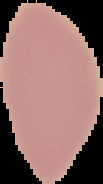

{
  "malaria_status": "uninfected",
  "preparation": "thin blood smear",
  "image_type": "cell region segmented out of the field of view; surrounding area masked to black",
  "image_size": "103×184 pixels"
}